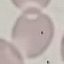
Summary:
  - Result: negative for malaria parasites
  - Stain: Giemsa
  - Capture: smartphone camera at the microscope eyepiece
  - Preparation: thin blood smear
  - Image type: cell patch, automatically extracted from a larger field of view and resized to 64 × 64 pixels